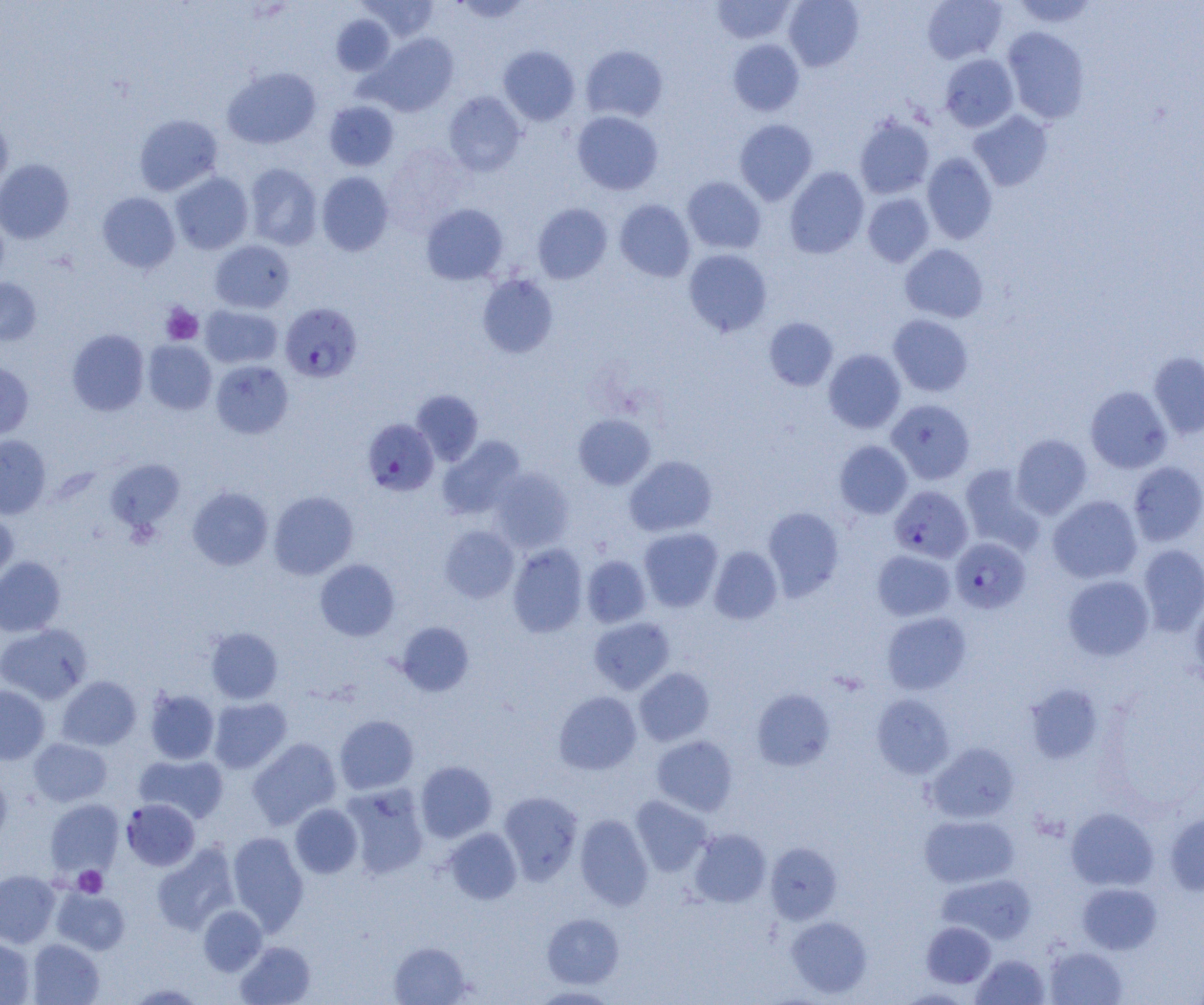
Approximate bounding boxes as (x1, y1, x2, y2) in pixels. Platelet locations: (161, 303, 203, 345), (73, 866, 107, 897). Plasmodium falciparum-infected red blood cell locations: (280, 302, 362, 383), (362, 418, 439, 496), (890, 485, 972, 563), (950, 537, 1031, 613), (121, 799, 200, 870). Uninfected red blood cell locations: (357, 0, 439, 41), (451, 0, 533, 23), (712, 0, 796, 44), (783, 0, 864, 71), (922, 0, 1007, 64), (1011, 0, 1099, 28), (331, 14, 395, 76), (1002, 27, 1090, 124), (366, 33, 459, 116), (728, 39, 804, 116), (499, 45, 580, 125), (580, 45, 668, 123), (939, 53, 1018, 131), (222, 67, 321, 149), (444, 91, 526, 176), (324, 100, 399, 171), (572, 110, 663, 195), (968, 110, 1053, 191), (134, 114, 222, 196), (0, 115, 13, 194), (854, 115, 934, 199), (734, 119, 818, 205), (383, 144, 470, 233), (922, 152, 997, 244), (0, 159, 74, 244), (244, 163, 323, 250), (784, 167, 869, 259), (317, 171, 394, 256), (170, 172, 254, 255), (682, 176, 766, 254), (97, 192, 180, 273), (863, 193, 934, 267), (614, 199, 696, 281), (421, 203, 508, 285), (533, 203, 612, 283), (210, 240, 295, 313), (899, 244, 988, 323), (683, 249, 772, 336), (477, 273, 558, 358), (0, 278, 41, 346), (200, 305, 282, 369), (888, 314, 973, 396), (764, 317, 838, 391), (67, 329, 149, 416), (143, 340, 217, 414), (823, 349, 906, 433), (1148, 352, 1204, 438), (0, 360, 34, 441), (210, 360, 293, 438), (1085, 386, 1172, 473), (411, 390, 483, 466), (886, 399, 975, 484), (573, 414, 655, 489), (1011, 434, 1092, 519), (0, 435, 51, 519), (437, 436, 525, 520), (835, 441, 912, 518), (624, 455, 717, 537), (105, 459, 185, 532), (1128, 461, 1204, 546), (960, 464, 1045, 554), (488, 467, 574, 553), (187, 486, 273, 571), (268, 491, 358, 579), (1048, 495, 1142, 583), (763, 507, 844, 600), (0, 511, 18, 589), (439, 525, 519, 603), (638, 528, 723, 612), (507, 543, 588, 638), (1137, 544, 1204, 636), (709, 546, 783, 625), (872, 549, 955, 621), (582, 555, 651, 628), (0, 556, 66, 636), (315, 559, 400, 641), (1062, 575, 1154, 660), (1190, 598, 1204, 688), (881, 611, 971, 694), (589, 616, 675, 694), (396, 621, 474, 697), (0, 623, 92, 704), (205, 627, 283, 703), (634, 667, 715, 746), (56, 676, 141, 750), (1025, 684, 1103, 763), (0, 685, 49, 764), (751, 688, 835, 771), (144, 689, 220, 764), (553, 691, 641, 775), (871, 694, 954, 779), (208, 697, 292, 773), (334, 715, 418, 794), (651, 735, 738, 816), (247, 737, 341, 829), (29, 738, 112, 806), (925, 742, 1019, 824), (135, 754, 229, 823), (415, 761, 497, 842), (0, 772, 13, 849), (341, 783, 430, 879), (498, 792, 583, 884), (630, 795, 711, 876), (45, 799, 123, 876), (290, 803, 363, 878), (1066, 807, 1158, 891), (1165, 812, 1204, 895), (574, 814, 653, 910), (919, 814, 1019, 888), (442, 828, 522, 904), (689, 828, 771, 907), (227, 831, 309, 934), (152, 842, 240, 935), (766, 842, 842, 924), (0, 869, 60, 947), (937, 873, 1037, 945), (1077, 883, 1161, 954), (51, 886, 130, 955), (198, 905, 267, 976), (542, 913, 624, 988), (786, 915, 872, 998), (921, 921, 996, 988), (0, 937, 35, 1004), (27, 939, 104, 1005), (235, 941, 315, 1005), (389, 941, 471, 1004), (1045, 946, 1127, 1004), (972, 954, 1050, 1004), (124, 982, 206, 1004), (529, 986, 621, 1004). Slide-level diagnosis: Plasmodium falciparum. Light microscopy. Image is 1204×1005 pixels. Thin blood smear. One field of a larger specimen. Captured at 1000x magnification.